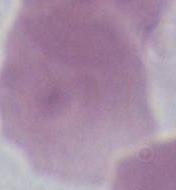

Summary:
  - Modality: photomicrograph
  - Identification: red blood cell
  - Magnification: 1000x